Point out each leukocyte.
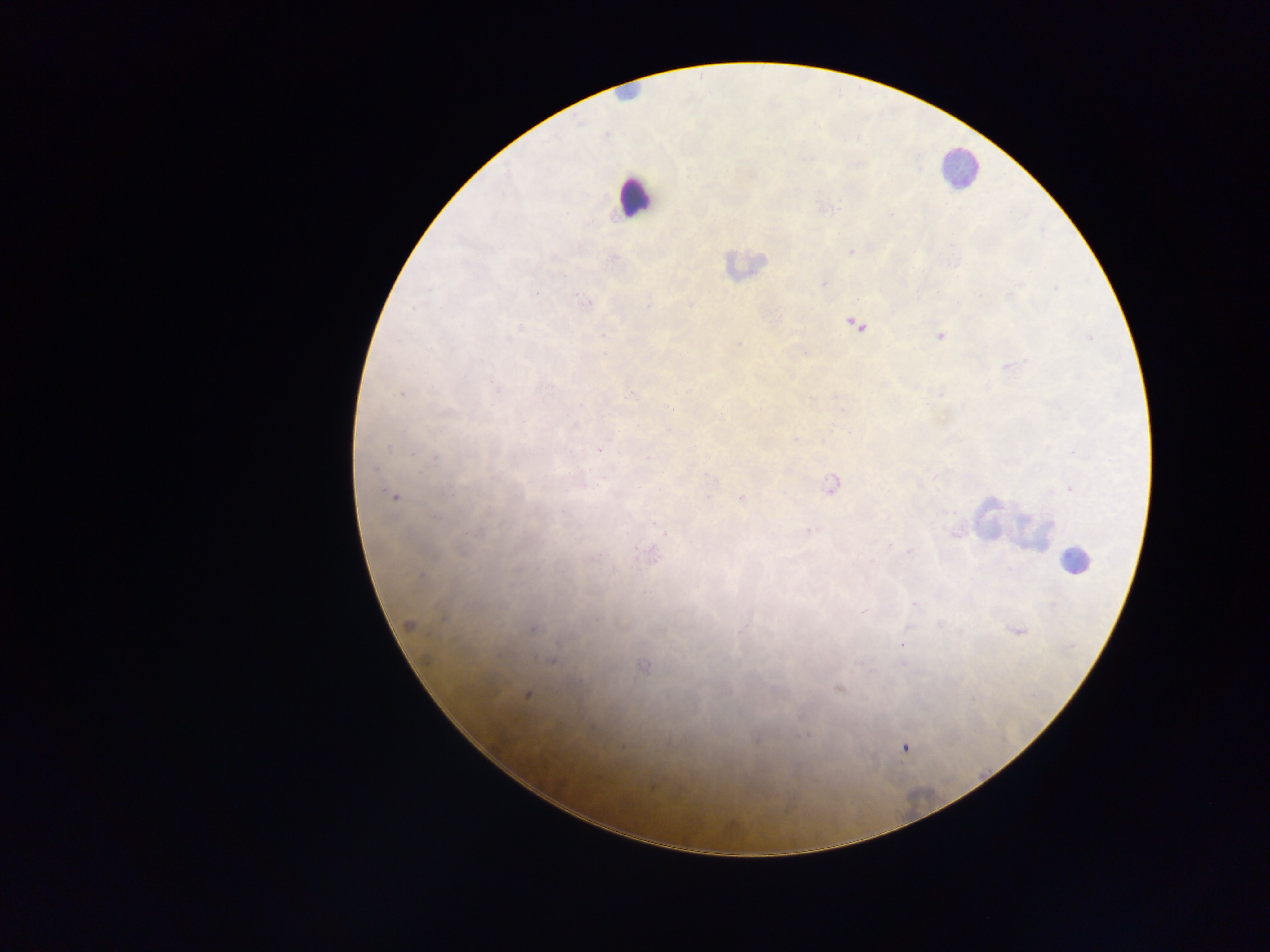
Approximate centers as {x, y} in pixels.
Leukocytes: {957, 167}, {634, 198}, {742, 264}, {989, 518}, {1034, 533}.
One object is labeled both Plasmodium parasite and leukocyte by the source: {1075, 560}.

preparation: thick blood film
capture: mobile-phone photograph through a microscope
image_size: 1270×952 pixels
plasmodium_parasite_locations: 'approximate centers as {x, y} in pixels: {891, 215}, {579, 246}, {851, 252}, {613, 258}, {824, 284}, {1056, 289}, {1011, 294}, {981, 295}, {586, 302}, {691, 304}, {647, 306}, {412, 308}, {855, 325}, {519, 326}, {603, 335}, {940, 335}, {1089, 337}, {739, 343}, {603, 355}, {1008, 366}, {493, 387}, {400, 394}, {632, 395}, {836, 397}, {810, 399}, {673, 409}, {760, 410}, {720, 413}, {576, 425}, {669, 430}, {796, 440}, {389, 449}, {599, 449}, {435, 458}, {374, 469}, {707, 476}, {935, 476}, {831, 485}, {1070, 489}, {394, 496}, {707, 497}, {742, 498}, {658, 526}, {479, 531}, {666, 531}, {809, 531}, {956, 533}, {909, 552}, {653, 555}, {914, 604}, {1052, 605}, {864, 611}, {409, 624}, {940, 624}, {907, 627}, {533, 628}, {1017, 630}, {551, 659}, {860, 663}, {901, 663}, {643, 667}, {839, 689}, {527, 694}, {804, 735}, {905, 748}'
field_of_view: single
country: Ghana